State which parasite is depicted.
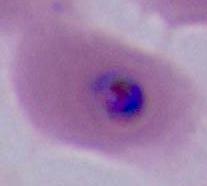

This is Plasmodium.

Captured at either 400x or 1000x magnification. Photomicrograph.